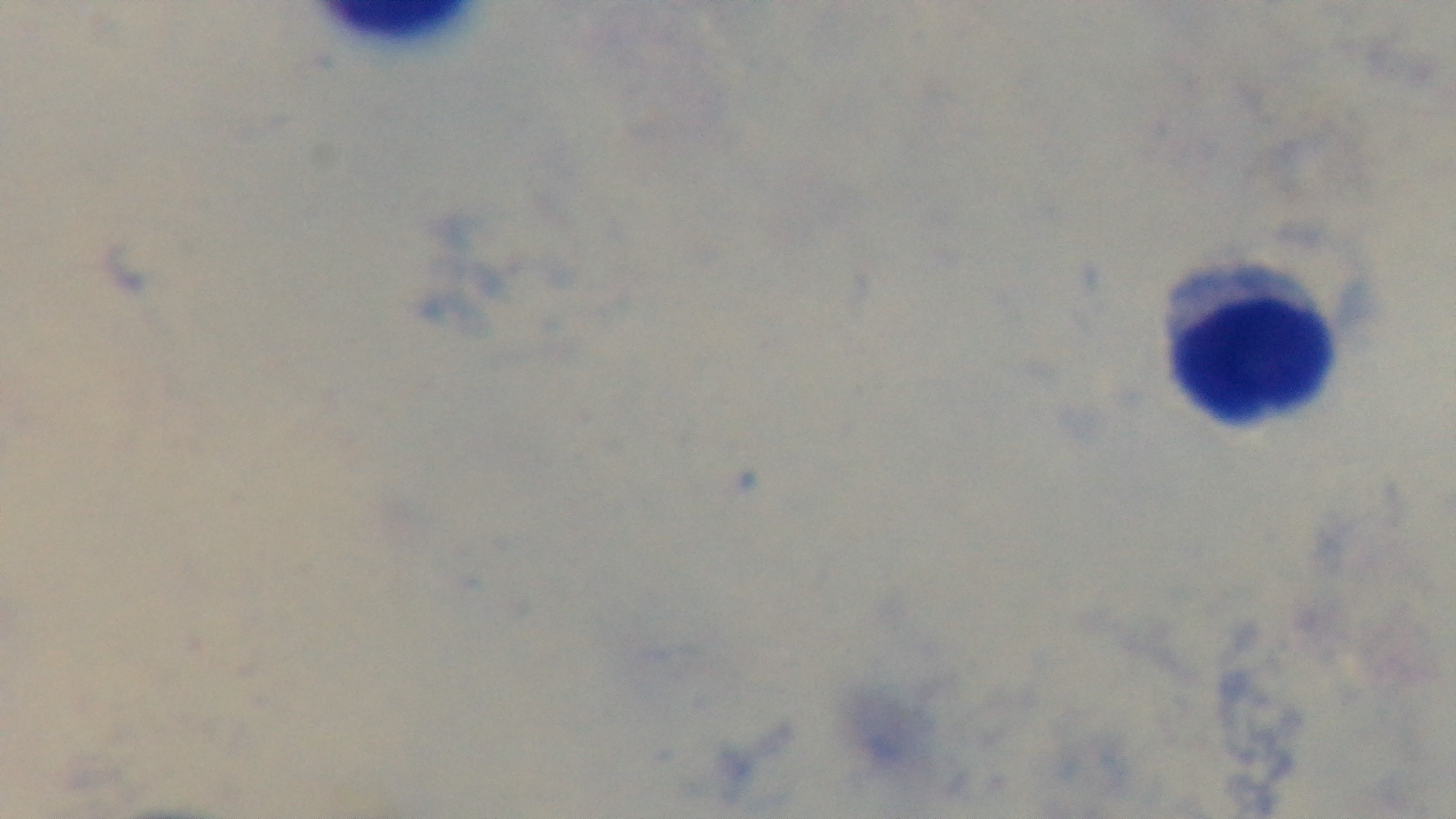
preparation = thick
objective = 100x oil immersion
malaria status = uninfected
capture = mounted 4K digital camera
modality = light microscopy
field of view = single
stain = Giemsa